Assess the morphology of the red blood cells.
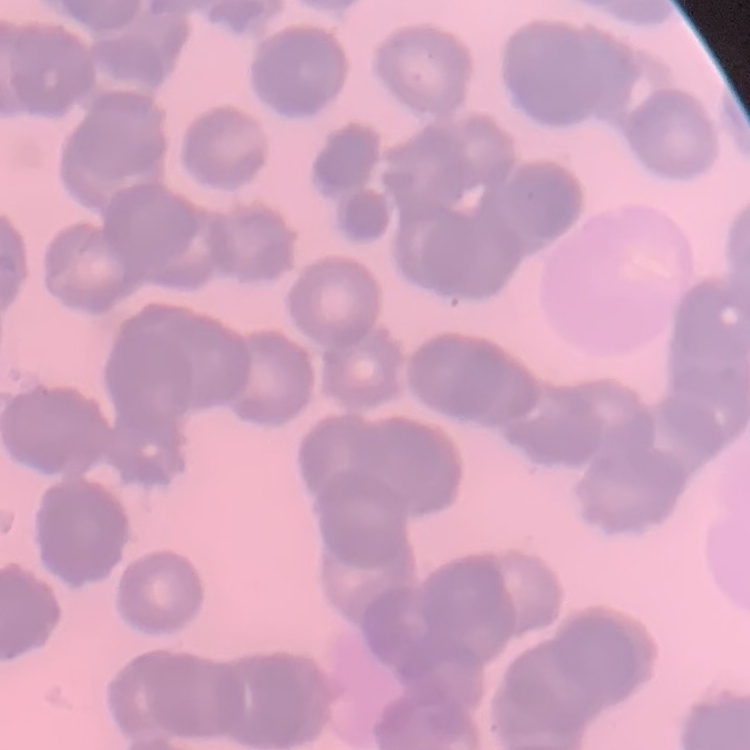
Rouleaux formation.

{
  "stain": "Field's or Giemsa",
  "preparation": "thin blood film",
  "image_type": "one tile cut from a larger photomicrograph"
}